State the blood parasite species.
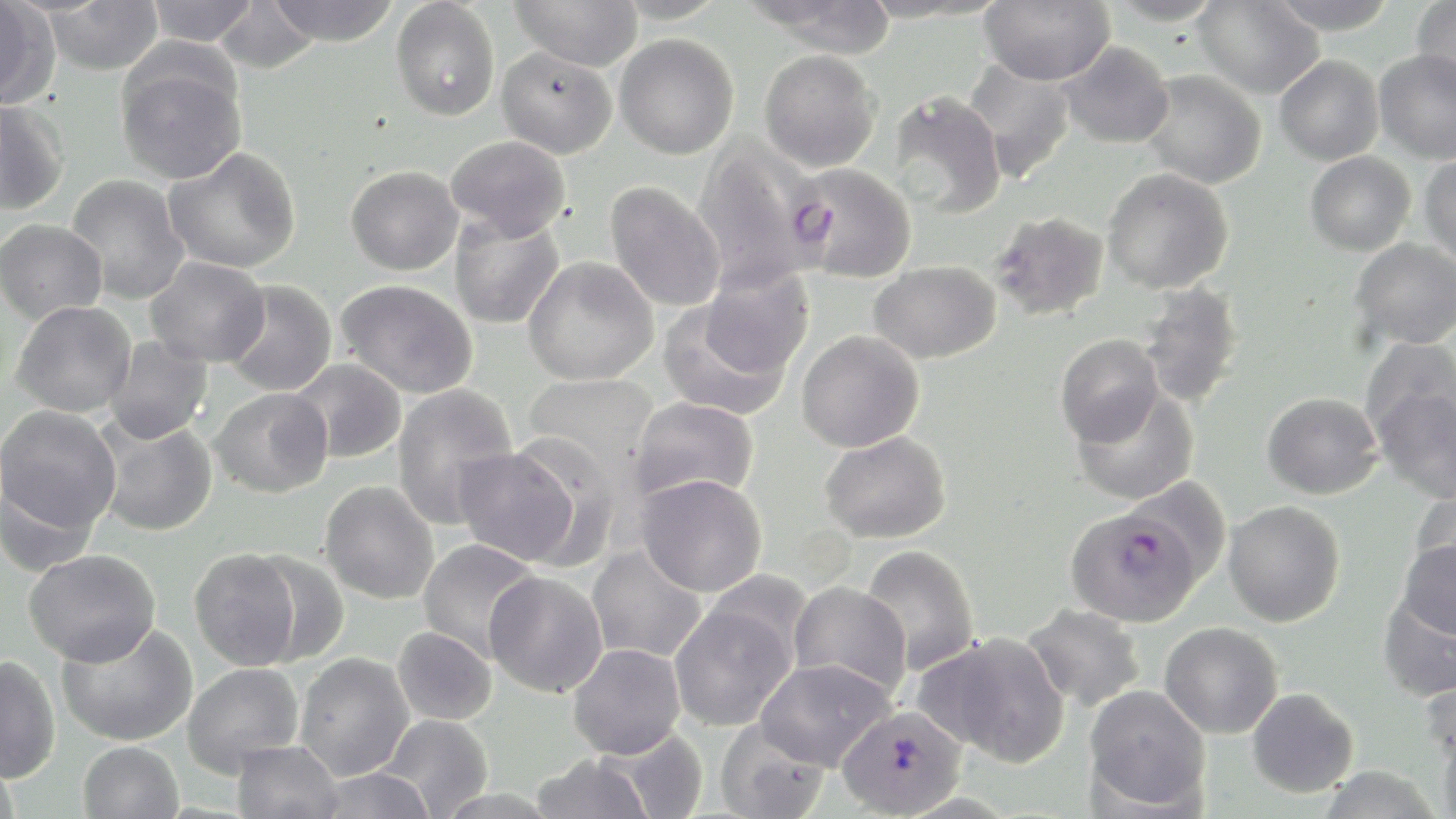
Plasmodium falciparum.

Approximate bounding boxes as named x1/y1/x2/y2 corners in pixels. Plasmodium falciparum-infected red blood cell locations: (x1=791, y1=162, x2=918, y2=282), (x1=1066, y1=504, x2=1202, y2=627), (x1=837, y1=705, x2=968, y2=818). Uninfected red blood cell locations: (x1=0, y1=0, x2=53, y2=106), (x1=144, y1=0, x2=260, y2=46), (x1=391, y1=0, x2=500, y2=121), (x1=509, y1=0, x2=643, y2=72), (x1=608, y1=0, x2=732, y2=24), (x1=750, y1=0, x2=900, y2=56), (x1=978, y1=0, x2=1116, y2=86), (x1=1103, y1=0, x2=1227, y2=26), (x1=1192, y1=0, x2=1324, y2=99), (x1=1266, y1=0, x2=1401, y2=35), (x1=1412, y1=0, x2=1456, y2=95), (x1=42, y1=1, x2=163, y2=75), (x1=213, y1=1, x2=320, y2=74), (x1=265, y1=1, x2=401, y2=46), (x1=615, y1=34, x2=739, y2=159), (x1=1057, y1=41, x2=1174, y2=148), (x1=497, y1=46, x2=617, y2=158), (x1=759, y1=49, x2=880, y2=171), (x1=1374, y1=49, x2=1456, y2=164), (x1=115, y1=54, x2=248, y2=185), (x1=1275, y1=55, x2=1384, y2=166), (x1=963, y1=59, x2=1078, y2=183), (x1=1138, y1=69, x2=1267, y2=189), (x1=887, y1=90, x2=1007, y2=218), (x1=0, y1=99, x2=68, y2=215), (x1=445, y1=135, x2=571, y2=241), (x1=691, y1=136, x2=830, y2=293), (x1=163, y1=147, x2=301, y2=274), (x1=1304, y1=151, x2=1416, y2=256), (x1=1419, y1=154, x2=1456, y2=268), (x1=346, y1=165, x2=463, y2=275), (x1=1103, y1=168, x2=1234, y2=294), (x1=65, y1=174, x2=191, y2=304), (x1=604, y1=181, x2=726, y2=313), (x1=990, y1=210, x2=1110, y2=321), (x1=449, y1=211, x2=564, y2=330), (x1=0, y1=219, x2=108, y2=323), (x1=1350, y1=238, x2=1456, y2=349), (x1=523, y1=256, x2=659, y2=386), (x1=145, y1=257, x2=269, y2=367), (x1=869, y1=260, x2=1002, y2=363), (x1=336, y1=279, x2=478, y2=399), (x1=222, y1=280, x2=337, y2=396), (x1=1137, y1=283, x2=1246, y2=408), (x1=657, y1=291, x2=801, y2=420), (x1=10, y1=300, x2=137, y2=418), (x1=797, y1=330, x2=925, y2=453), (x1=1055, y1=333, x2=1164, y2=447), (x1=104, y1=335, x2=213, y2=445), (x1=1360, y1=337, x2=1455, y2=447), (x1=290, y1=358, x2=406, y2=463), (x1=523, y1=373, x2=659, y2=478), (x1=392, y1=383, x2=518, y2=528), (x1=210, y1=387, x2=333, y2=498), (x1=1070, y1=388, x2=1200, y2=506), (x1=1375, y1=388, x2=1456, y2=502), (x1=1262, y1=392, x2=1383, y2=499), (x1=627, y1=396, x2=760, y2=507), (x1=0, y1=405, x2=121, y2=535), (x1=96, y1=419, x2=218, y2=537), (x1=819, y1=430, x2=952, y2=544), (x1=508, y1=435, x2=626, y2=569), (x1=453, y1=444, x2=582, y2=566), (x1=636, y1=473, x2=767, y2=596), (x1=0, y1=477, x2=100, y2=577), (x1=320, y1=480, x2=439, y2=604), (x1=1409, y1=490, x2=1456, y2=592), (x1=1223, y1=500, x2=1345, y2=627), (x1=417, y1=538, x2=540, y2=661), (x1=1397, y1=538, x2=1456, y2=640), (x1=859, y1=544, x2=980, y2=676), (x1=587, y1=545, x2=707, y2=663), (x1=189, y1=548, x2=303, y2=670), (x1=23, y1=549, x2=160, y2=667), (x1=245, y1=550, x2=351, y2=666), (x1=484, y1=571, x2=608, y2=697), (x1=788, y1=582, x2=911, y2=699), (x1=1378, y1=590, x2=1455, y2=701), (x1=669, y1=601, x2=798, y2=733), (x1=1022, y1=604, x2=1146, y2=711), (x1=56, y1=620, x2=197, y2=746), (x1=1160, y1=621, x2=1283, y2=739), (x1=392, y1=626, x2=497, y2=725), (x1=918, y1=631, x2=1071, y2=766), (x1=568, y1=644, x2=685, y2=759), (x1=295, y1=652, x2=415, y2=780), (x1=0, y1=655, x2=60, y2=783), (x1=755, y1=658, x2=895, y2=770), (x1=183, y1=663, x2=303, y2=776), (x1=1420, y1=670, x2=1456, y2=774), (x1=1084, y1=684, x2=1211, y2=812), (x1=1247, y1=688, x2=1358, y2=797), (x1=376, y1=714, x2=494, y2=818), (x1=714, y1=719, x2=830, y2=819), (x1=591, y1=726, x2=710, y2=819), (x1=1438, y1=728, x2=1456, y2=819), (x1=231, y1=739, x2=344, y2=819), (x1=78, y1=741, x2=184, y2=818), (x1=0, y1=751, x2=22, y2=819), (x1=529, y1=753, x2=655, y2=819), (x1=315, y1=767, x2=438, y2=818). Thin blood smear. May-Grünwald-Giemsa-stained preparation. Captured at 1000x magnification. Optical microscopy. Image is 1456×819 pixels. Single field of view.